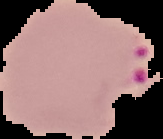 From a thin blood film. Image is 163×139 pixels. Result: Plasmodium parasites identified. Cell region segmented out of the field of view; the surrounding area is masked to black.